Comment on the morphology of the red blood cells.
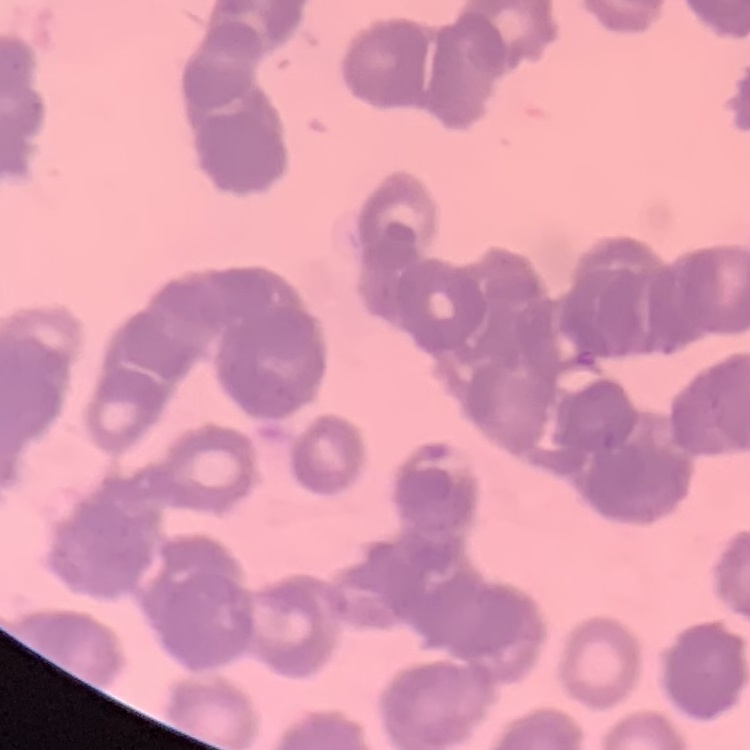
They show rouleaux formation.

Thin peripheral smear. Square crop of a larger photomicrograph. Stained with either Field's or Giemsa.